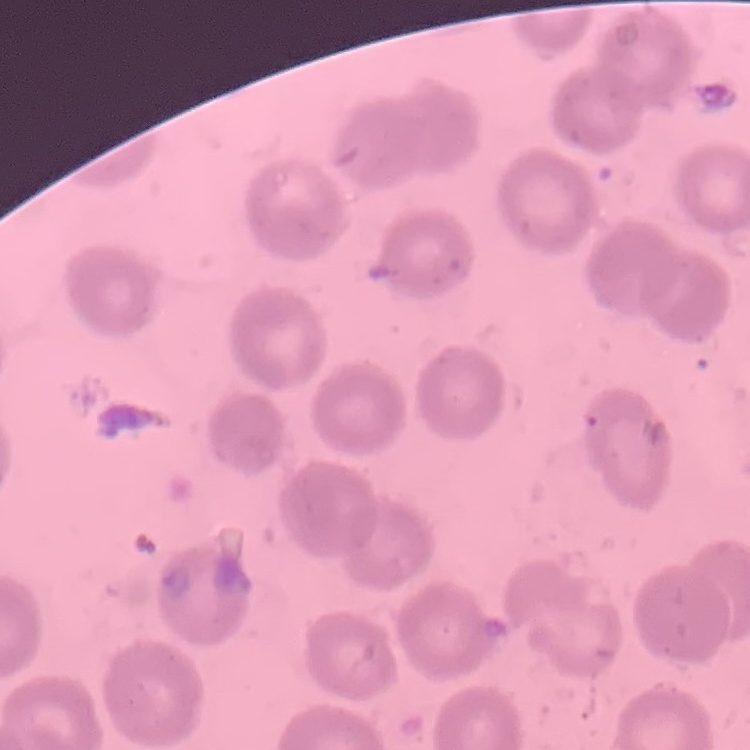
Summary:
  - Red blood cell morphology: no rouleaux formation
  - Stain: Field's or Giemsa
  - Image type: square crop of a larger photomicrograph
  - Preparation: thin blood smear